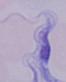 Captured at 1000x magnification. A trypanosome is shown. Photomicrograph.